Give the extent of all Babesia divergens-infected red blood cells.
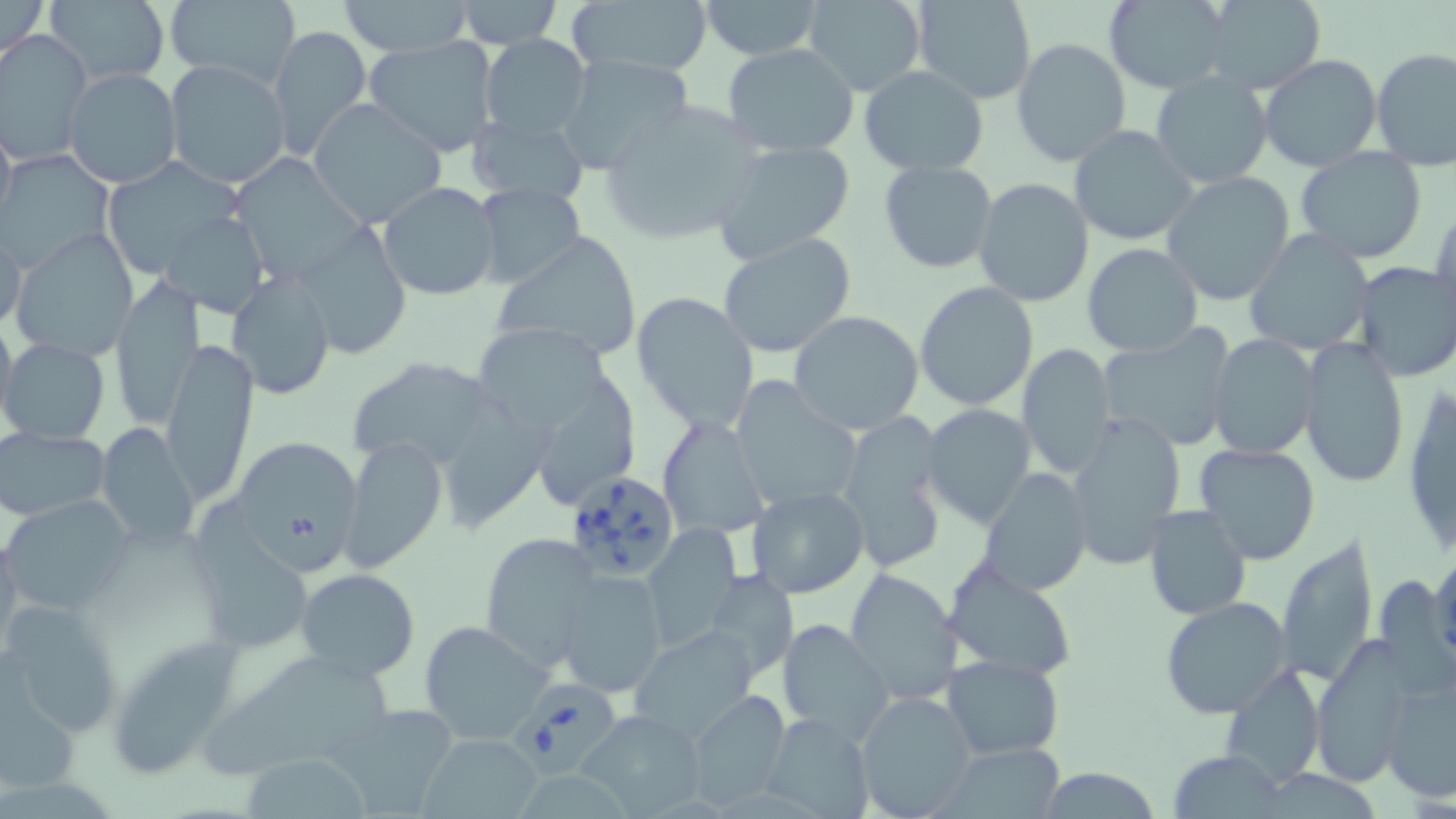
Approximate bounding boxes as (x1, y1, x2, y2) in pixels.
Babesia divergens-infected red blood cells: (564, 467, 680, 583), (507, 674, 624, 777).

Uninfected red blood cell locations: (0, 0, 47, 61), (44, 0, 172, 88), (338, 0, 475, 58), (453, 0, 562, 47), (801, 0, 928, 96), (911, 0, 1037, 105), (1102, 0, 1237, 92), (1196, 0, 1328, 95), (165, 1, 299, 87), (697, 1, 823, 60), (566, 2, 712, 82), (266, 25, 371, 160), (1, 30, 94, 163), (480, 34, 592, 143), (364, 35, 498, 156), (1012, 37, 1132, 167), (721, 44, 861, 156), (1372, 47, 1456, 170), (555, 53, 696, 173), (1259, 54, 1381, 172), (164, 59, 289, 189), (63, 67, 181, 189), (859, 67, 989, 176), (1150, 71, 1273, 191), (307, 98, 448, 228), (596, 100, 767, 246), (0, 107, 16, 236), (465, 114, 590, 209), (1069, 124, 1201, 247), (715, 141, 854, 260), (1295, 146, 1429, 265), (0, 150, 119, 271), (229, 152, 370, 285), (99, 155, 250, 278), (879, 160, 997, 273), (1162, 171, 1296, 306), (973, 178, 1095, 307), (377, 181, 502, 302), (473, 183, 588, 292), (1433, 198, 1456, 328), (156, 209, 271, 319), (293, 221, 412, 359), (0, 225, 27, 335), (1244, 228, 1374, 356), (11, 229, 139, 360), (491, 230, 640, 361), (717, 232, 859, 358), (1082, 243, 1203, 357), (1352, 261, 1455, 382), (226, 271, 336, 398), (109, 274, 203, 432), (914, 282, 1039, 412), (631, 290, 760, 436), (792, 297, 1040, 420), (130, 303, 237, 471), (789, 310, 924, 435), (472, 313, 622, 432), (1097, 327, 1237, 451), (1209, 333, 1320, 460), (2, 337, 109, 443), (1299, 337, 1410, 487), (159, 341, 258, 505), (1018, 343, 1115, 477), (348, 358, 504, 473), (538, 364, 646, 502), (451, 372, 567, 532), (730, 378, 862, 516), (1403, 378, 1455, 559), (921, 404, 1037, 527), (833, 408, 951, 571), (1064, 412, 1187, 570), (655, 413, 768, 541), (94, 423, 200, 550), (1, 426, 110, 524), (339, 436, 447, 574), (230, 438, 364, 574), (1193, 444, 1323, 566), (978, 468, 1092, 596), (747, 485, 870, 599), (2, 496, 133, 616), (1142, 506, 1251, 620), (642, 524, 742, 647), (194, 532, 319, 657), (478, 533, 603, 669), (1276, 536, 1381, 686), (1430, 550, 1456, 670), (942, 559, 1078, 683), (844, 567, 964, 705), (294, 568, 421, 679), (699, 570, 800, 682), (556, 571, 667, 698), (1160, 596, 1293, 719), (2, 602, 124, 738), (776, 618, 895, 743), (419, 620, 552, 745), (628, 626, 762, 740), (106, 631, 251, 779), (1312, 638, 1416, 784), (207, 647, 397, 777), (942, 655, 1063, 760), (1221, 664, 1326, 787), (1381, 671, 1456, 803), (686, 691, 789, 810), (854, 693, 978, 815), (326, 704, 459, 817), (577, 709, 709, 817), (760, 712, 872, 818), (421, 731, 543, 817), (942, 741, 1069, 818), (1172, 751, 1286, 817), (242, 754, 369, 818), (1034, 768, 1164, 819). Slide-level diagnosis: Babesia divergens. Light microscopy. Image is 1456×819 pixels. Captured at 1000x magnification. Thin blood smear. One field of a larger specimen. May-Grünwald-Giemsa stain.